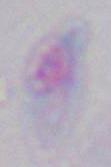

Summary:
  - Magnification: 1000x
  - Identification: Toxoplasma gondii
  - Modality: micrograph